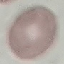
Result: no malaria parasites seen. Acquired by smartphone through the microscope eyepiece. Thin smear of blood. Cell patch, automatically extracted from a larger field of view and resized to 64 × 64 pixels. Giemsa stain.